Assess this cell for malaria.
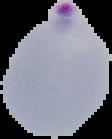
Parasitized.

Image is 112×139 pixels. Cell region segmented out of the field of view; the surrounding area is masked to black. From a thin blood film.